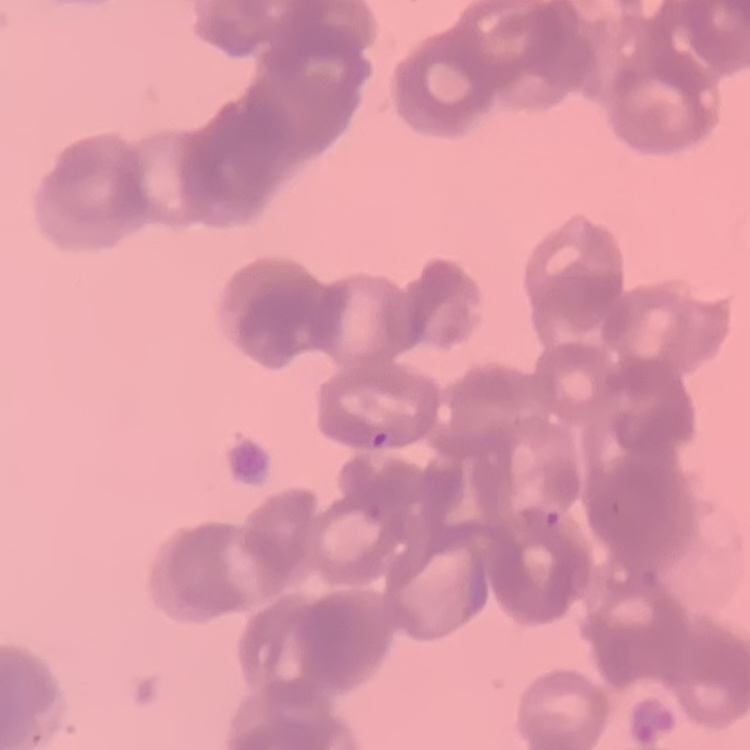

erythrocyte morphology = rouleaux formation
image type = one tile cut from a larger photomicrograph
preparation = thin peripheral smear
stain = Field's or Giemsa